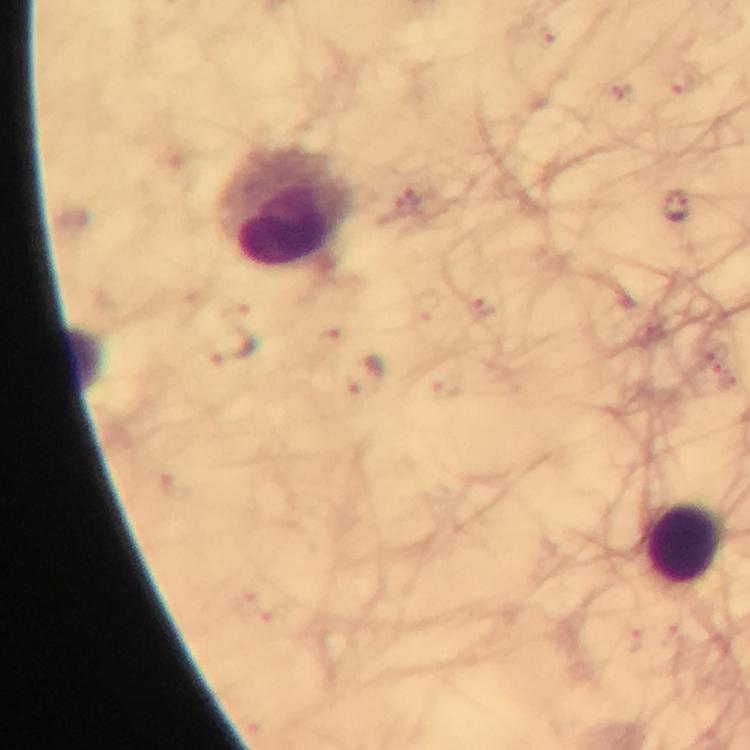

Approximate centers as {x, y} in pixels. Leukocyte locations: {289, 207}, {685, 543}. Malaria parasite locations: {676, 209}, {232, 351}, {366, 376}. 100x magnification. From a diagnostic examination for malaria. Giemsa-stained preparation. Image is 750×750 pixels. Photographed through the microscope with a smartphone camera. Immersion oil applied. Thick blood film. Cropped region of a single field of view.